Give the position of every malaria parasite.
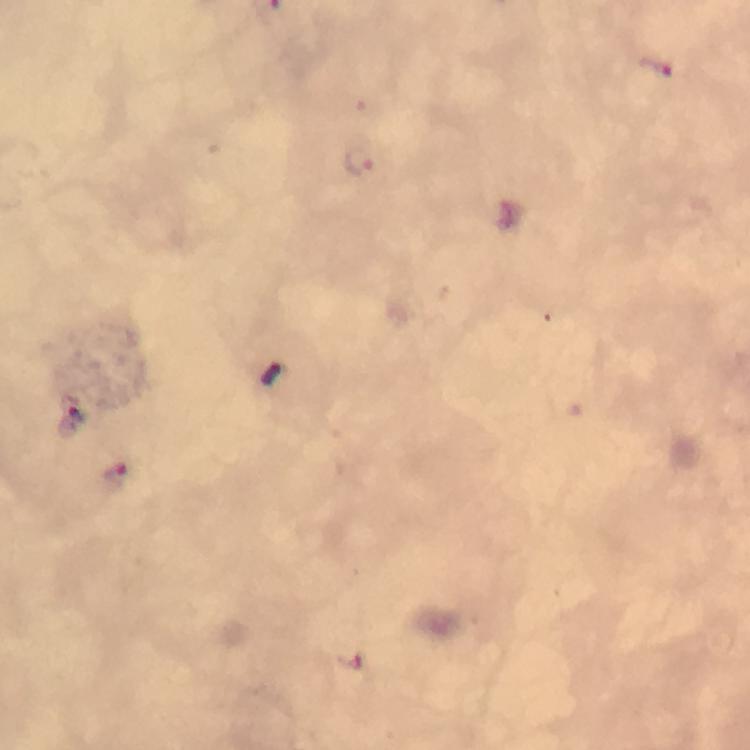

Approximate centers as {x, y} in pixels.
Malaria parasites: {657, 65}, {362, 167}, {277, 377}, {74, 417}, {114, 475}, {353, 665}.

cropped from = a single field of view
stain = Giemsa
context = from a diagnostic examination for malaria
immersion oil = used
capture = smartphone mounted on the microscope
image size = 750×750 pixels
preparation = thick smear
magnification = 100x